Mark where platelets are.
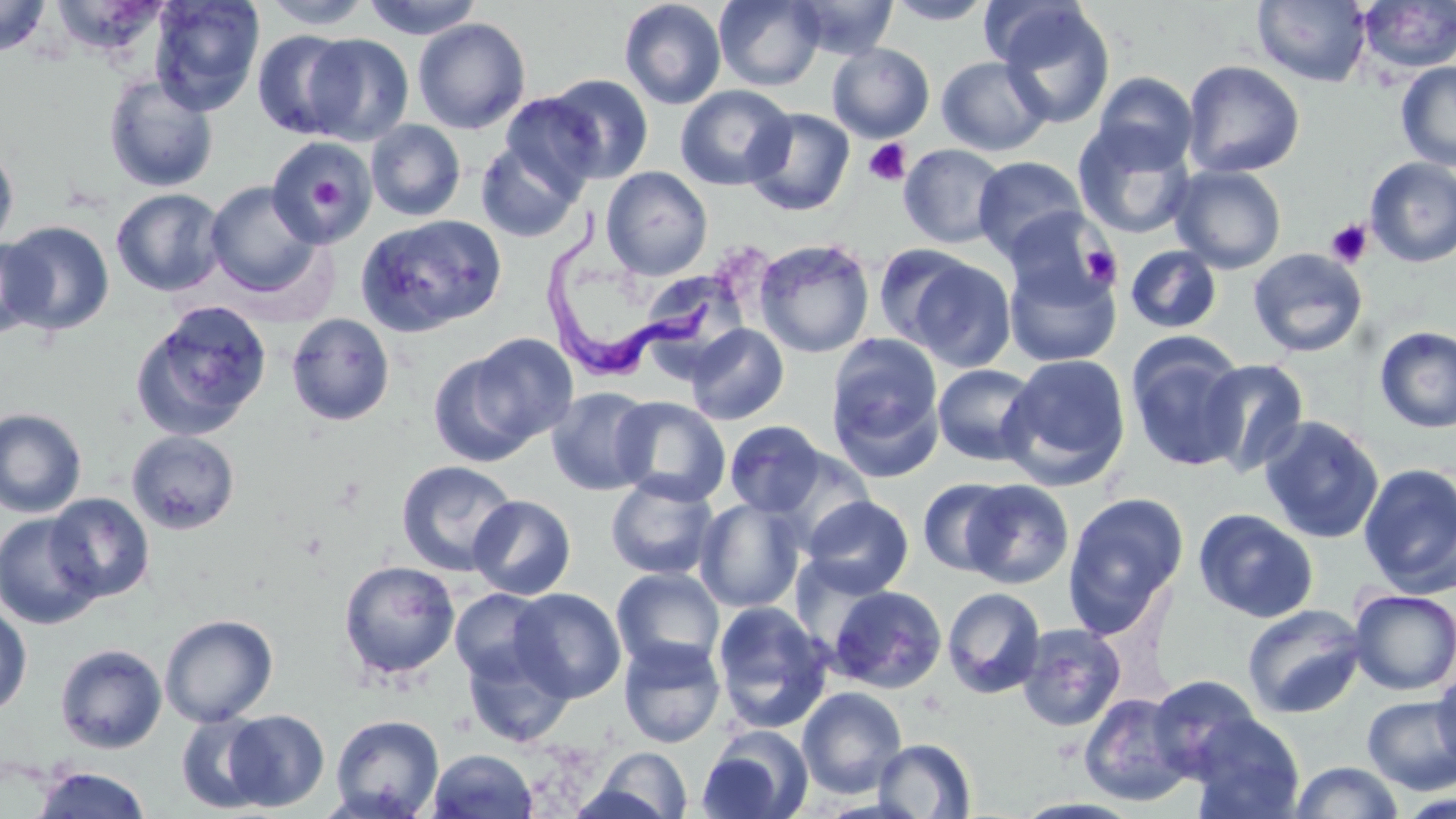
Approximate bounding boxes as [x1, y1, x2, y2] in pixels.
Platelets: [864, 138, 911, 186], [300, 165, 352, 222], [1325, 219, 1373, 268], [1081, 245, 1121, 287].

slide-level diagnosis = Trypanosoma brucei
magnification = 1000x
Trypanosoma brucei locations = approximate bounding boxes as [x1, y1, x2, y2] in pixels: [546, 206, 720, 384]
stain = May-Grünwald-Giemsa
image size = 1456×819 pixels
field of view = single
preparation = thin blood smear
modality = optical microscopy
uninfected red blood cell locations = approximate bounding boxes as [x1, y1, x2, y2] in pixels: [0, 0, 51, 57], [149, 0, 265, 115], [259, 0, 376, 30], [362, 0, 485, 39], [619, 0, 727, 110], [713, 0, 825, 90], [788, 0, 899, 59], [884, 0, 996, 24], [1252, 0, 1371, 87], [980, 1, 1089, 70], [1357, 1, 1456, 73], [995, 4, 1117, 130], [412, 17, 531, 134], [253, 29, 359, 140], [302, 33, 414, 145], [826, 43, 935, 143], [936, 56, 1052, 156], [1182, 60, 1304, 178], [1395, 61, 1456, 171], [1092, 72, 1198, 172], [544, 73, 654, 184], [103, 74, 219, 193], [675, 84, 795, 190], [500, 93, 604, 195], [744, 108, 855, 217], [365, 120, 466, 221], [1073, 123, 1196, 240], [265, 135, 377, 250], [474, 140, 584, 242], [0, 143, 19, 253], [899, 143, 1008, 249], [972, 156, 1088, 262], [1365, 157, 1456, 267], [1169, 165, 1287, 273], [601, 166, 713, 280], [205, 182, 323, 298], [111, 188, 227, 296], [1003, 207, 1117, 308], [355, 214, 508, 338], [3, 221, 114, 335], [0, 236, 48, 339], [752, 238, 875, 358], [872, 243, 979, 349], [1125, 245, 1222, 334], [1248, 248, 1368, 358], [904, 255, 1016, 371], [1003, 258, 1122, 367], [649, 273, 753, 383], [131, 302, 272, 442], [286, 314, 395, 426], [684, 323, 789, 425], [1373, 325, 1456, 434], [455, 332, 580, 452], [824, 333, 944, 476], [1126, 334, 1249, 471], [999, 353, 1132, 490], [1197, 359, 1309, 478], [932, 363, 1042, 466], [546, 387, 657, 496], [610, 396, 731, 505], [0, 407, 87, 518], [1258, 415, 1384, 544], [724, 421, 828, 518], [127, 430, 240, 535], [764, 446, 878, 551], [396, 460, 519, 576], [1358, 462, 1456, 597], [606, 475, 719, 580], [918, 477, 1018, 577], [961, 479, 1074, 588], [1062, 492, 1188, 635], [45, 493, 155, 602], [468, 494, 576, 600], [802, 495, 913, 598], [694, 498, 807, 613], [1193, 508, 1319, 623], [0, 513, 104, 630], [338, 559, 460, 680], [611, 567, 726, 675], [828, 584, 946, 693], [942, 587, 1046, 699], [449, 588, 555, 687], [509, 588, 626, 702], [1349, 588, 1456, 695], [711, 601, 833, 733], [1241, 603, 1366, 719], [0, 605, 32, 717], [160, 614, 278, 727], [1016, 623, 1126, 731], [460, 637, 576, 748], [618, 637, 727, 748], [55, 644, 167, 753], [1431, 667, 1456, 777], [1147, 675, 1264, 782], [797, 686, 908, 798], [1078, 692, 1194, 806], [1362, 694, 1455, 794], [223, 709, 330, 811], [175, 712, 275, 814], [329, 714, 445, 819], [1187, 714, 1305, 819], [697, 727, 812, 819], [871, 738, 977, 818], [587, 746, 693, 818], [427, 749, 538, 819], [1289, 761, 1404, 819], [31, 766, 153, 817], [1395, 792, 1456, 819]